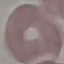
result = no malaria parasites detected
image type = cell patch, automatically extracted from a larger field of view and resized to 64 × 64 pixels
stain = Giemsa
preparation = thin blood smear
capture = smartphone through the microscope eyepiece